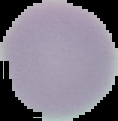
Summary:
  - Image size: 118×121 pixels
  - Image type: segmented cell region with the area outside set to black
  - Preparation: thin blood film
  - Malaria status: uninfected